Report the malaria status.
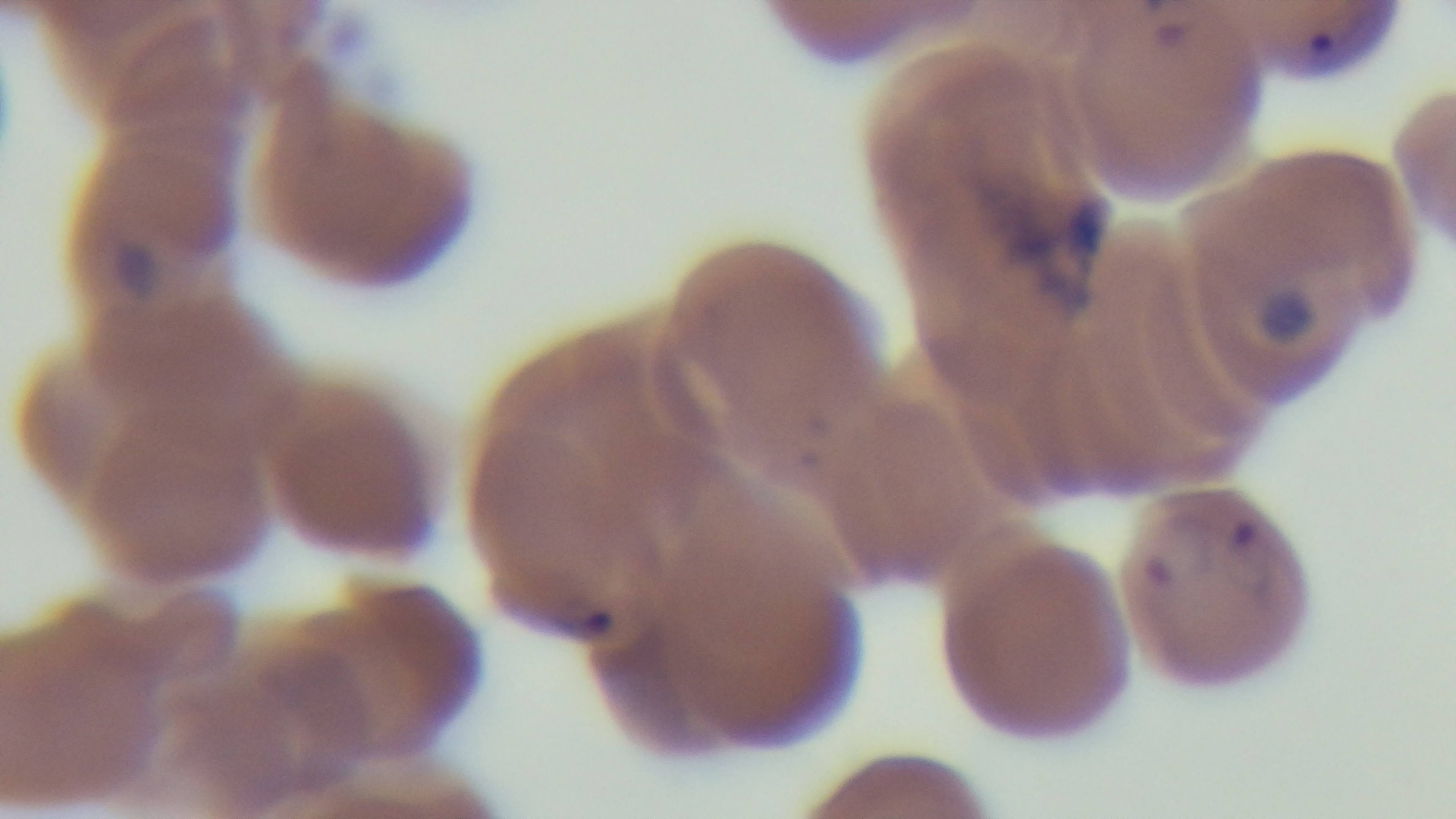

Infected.

Light microscopy. Giemsa stain. Preparation: thin smear. Mounted 4K digital camera. 100x oil-immersion objective. Single field of view.